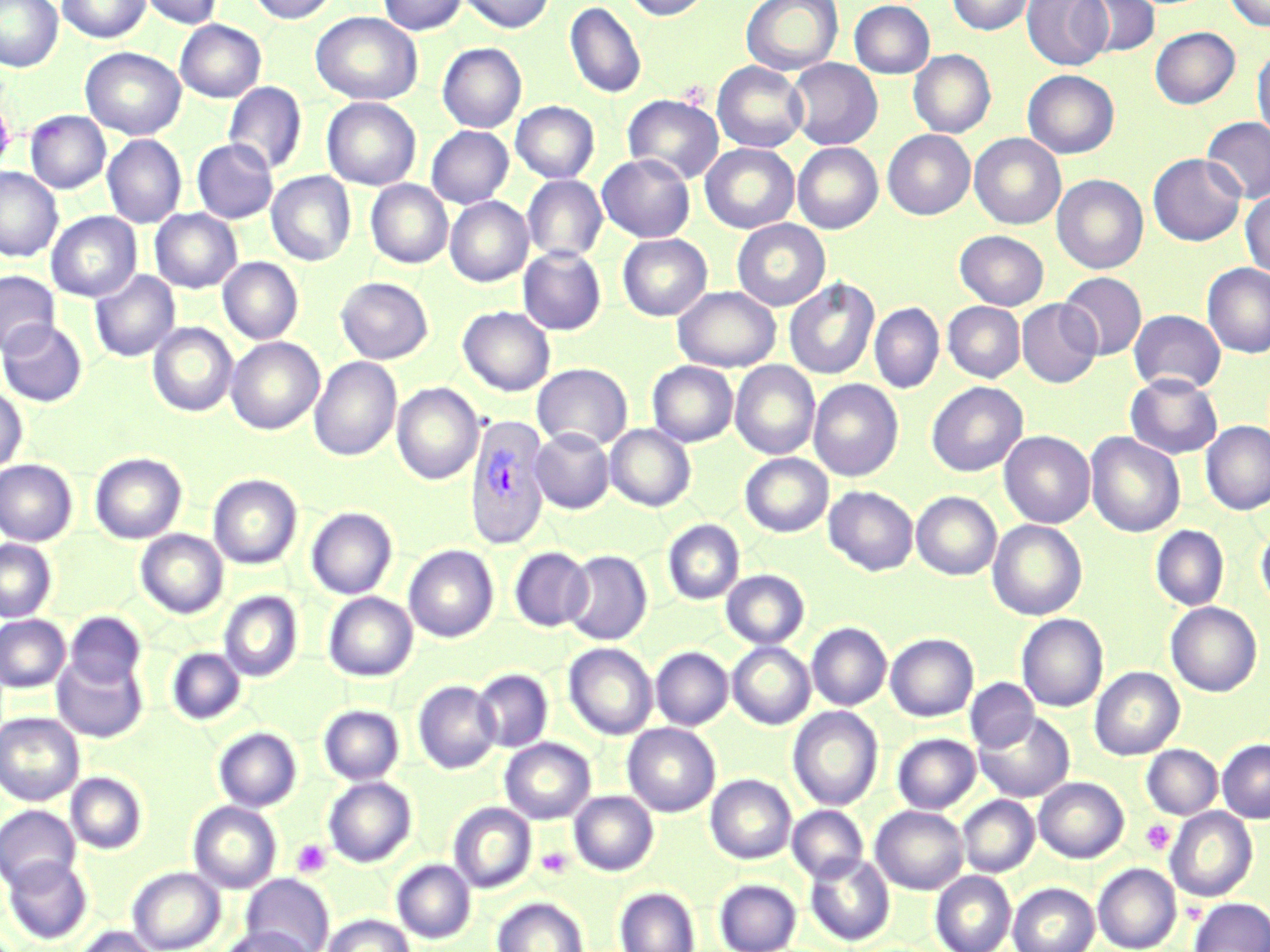

Summary:
  - Coordinate format: approximate bounding boxes as (x1, y1, x2, y2) in pixels
  - Plasmodium vivax-infected red blood cell locations: (463, 413, 553, 549)
  - Uninfected red blood cell locations: (0, 0, 63, 72), (57, 0, 151, 43), (137, 0, 224, 29), (248, 0, 339, 24), (378, 0, 467, 35), (459, 0, 556, 34), (623, 0, 711, 21), (741, 0, 843, 75), (947, 0, 1034, 36), (1022, 0, 1112, 70), (1079, 0, 1160, 58), (1224, 0, 1270, 31), (565, 1, 647, 99), (849, 1, 935, 79), (311, 11, 422, 105), (175, 20, 266, 102), (1150, 27, 1240, 109), (437, 43, 526, 132), (1252, 46, 1270, 144), (80, 47, 186, 139), (908, 50, 996, 138), (786, 58, 882, 150), (712, 61, 808, 153), (1023, 70, 1119, 159), (223, 82, 307, 175), (623, 94, 724, 184), (322, 98, 421, 190), (511, 101, 599, 183), (26, 111, 110, 194), (1201, 117, 1270, 205), (426, 126, 513, 208), (883, 130, 975, 220), (969, 133, 1066, 229), (103, 135, 186, 228), (192, 139, 278, 223), (793, 142, 883, 233), (701, 143, 799, 232), (1148, 153, 1246, 246), (598, 154, 695, 243), (0, 167, 63, 262), (520, 170, 695, 259), (267, 171, 355, 266), (1052, 174, 1148, 274), (522, 175, 607, 263), (366, 180, 453, 268), (1240, 190, 1270, 279), (445, 197, 533, 287), (150, 209, 242, 293), (46, 212, 141, 302), (731, 220, 830, 311), (955, 230, 1049, 310), (617, 234, 712, 321), (518, 246, 606, 335), (218, 257, 303, 344), (1201, 263, 1270, 358), (90, 270, 180, 362), (0, 271, 59, 357), (1058, 272, 1146, 360), (336, 277, 433, 363), (784, 278, 879, 380), (673, 286, 780, 372), (1016, 299, 1102, 388), (943, 301, 1025, 382), (869, 303, 944, 393), (458, 306, 556, 396), (1129, 310, 1226, 394), (0, 320, 87, 407), (148, 323, 238, 416), (226, 337, 324, 434), (309, 357, 401, 462), (648, 361, 738, 446), (731, 361, 820, 459), (532, 363, 632, 451), (1125, 373, 1223, 459), (808, 379, 903, 481), (927, 381, 1027, 477), (392, 382, 484, 485), (0, 386, 28, 475), (1200, 421, 1270, 515), (606, 424, 696, 511), (530, 428, 614, 513), (999, 431, 1095, 528), (1085, 432, 1185, 537), (90, 452, 187, 543), (740, 453, 832, 537), (0, 460, 77, 545), (208, 474, 302, 569), (824, 486, 918, 576), (912, 491, 1002, 580), (306, 507, 397, 599), (663, 519, 745, 604), (987, 520, 1087, 620), (1256, 523, 1270, 613), (1151, 525, 1229, 611), (136, 530, 228, 618), (0, 539, 57, 622), (404, 545, 499, 642), (509, 547, 592, 631), (563, 550, 652, 644), (721, 570, 809, 648), (219, 591, 303, 682), (323, 592, 417, 681), (1166, 602, 1262, 696), (64, 611, 146, 689), (1017, 613, 1108, 711), (0, 615, 70, 692), (807, 622, 891, 710), (885, 633, 979, 721), (728, 641, 815, 729), (563, 643, 657, 739), (167, 647, 246, 724), (651, 647, 733, 730), (52, 654, 148, 743), (1090, 667, 1184, 760), (472, 668, 553, 752), (965, 678, 1039, 753), (413, 680, 501, 774), (319, 705, 404, 784), (788, 707, 883, 810), (974, 711, 1075, 802), (0, 712, 84, 805), (623, 724, 720, 816), (214, 727, 302, 811), (892, 734, 981, 813), (500, 738, 595, 824), (1218, 739, 1270, 823), (1142, 744, 1222, 819), (66, 772, 147, 854), (706, 774, 796, 864), (323, 777, 416, 867), (1034, 777, 1129, 863), (569, 791, 658, 875), (957, 795, 1039, 877), (188, 801, 281, 893), (449, 802, 536, 893), (0, 805, 80, 891), (787, 805, 868, 883), (870, 805, 968, 894), (1165, 807, 1257, 901), (805, 854, 894, 946), (2, 856, 92, 944), (392, 859, 475, 943), (1093, 863, 1182, 952), (128, 866, 225, 952), (931, 871, 1016, 952), (714, 873, 895, 950), (243, 874, 334, 952), (714, 879, 802, 952), (1008, 882, 1099, 952), (615, 886, 700, 952), (492, 897, 588, 952), (1189, 897, 1270, 952), (323, 913, 414, 952), (220, 925, 317, 952), (73, 926, 160, 952)
  - Platelet locations: (1140, 819, 1175, 854), (290, 839, 331, 877), (536, 846, 573, 879)
  - Slide-level diagnosis: Plasmodium vivax
  - Preparation: thin blood smear
  - Field of view: one of a larger specimen
  - Stain: May-Grünwald-Giemsa
  - Modality: optical microscopy
  - Magnification: 1000x
  - Image size: 1270×952 pixels